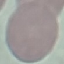

result = no malaria parasites seen
preparation = thin blood film
capture = smartphone camera at the microscope eyepiece
stain = Giemsa
image type = automatically extracted cell patch, resized to 64 × 64 pixels